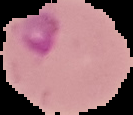

The area outside the segmented cell region is set to black. Image is 133×115 pixels. From a thin blood film. Malaria status: parasitized.